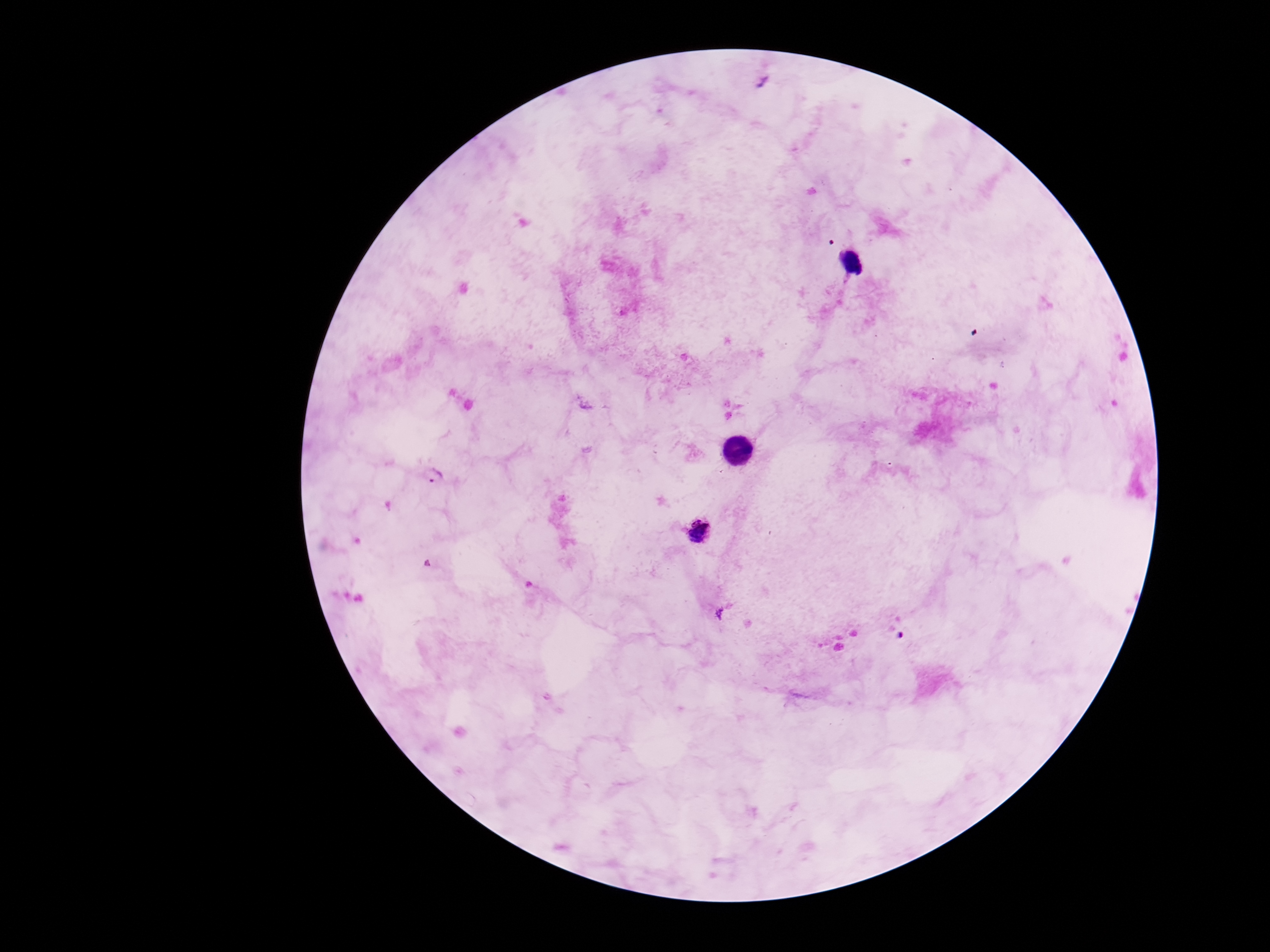
Approximate centers as [x, y] in pixels. Plasmodium parasite locations: [763, 80], [434, 474], [699, 532], [720, 613]. Image is 1270×952 pixels. Smartphone photograph taken through the microscope eyepiece. 100x magnification. Giemsa-stained preparation. One field from this slide. Thick peripheral-blood smear. Patient malaria status: positive.